Outline each blood parasite and name the species.
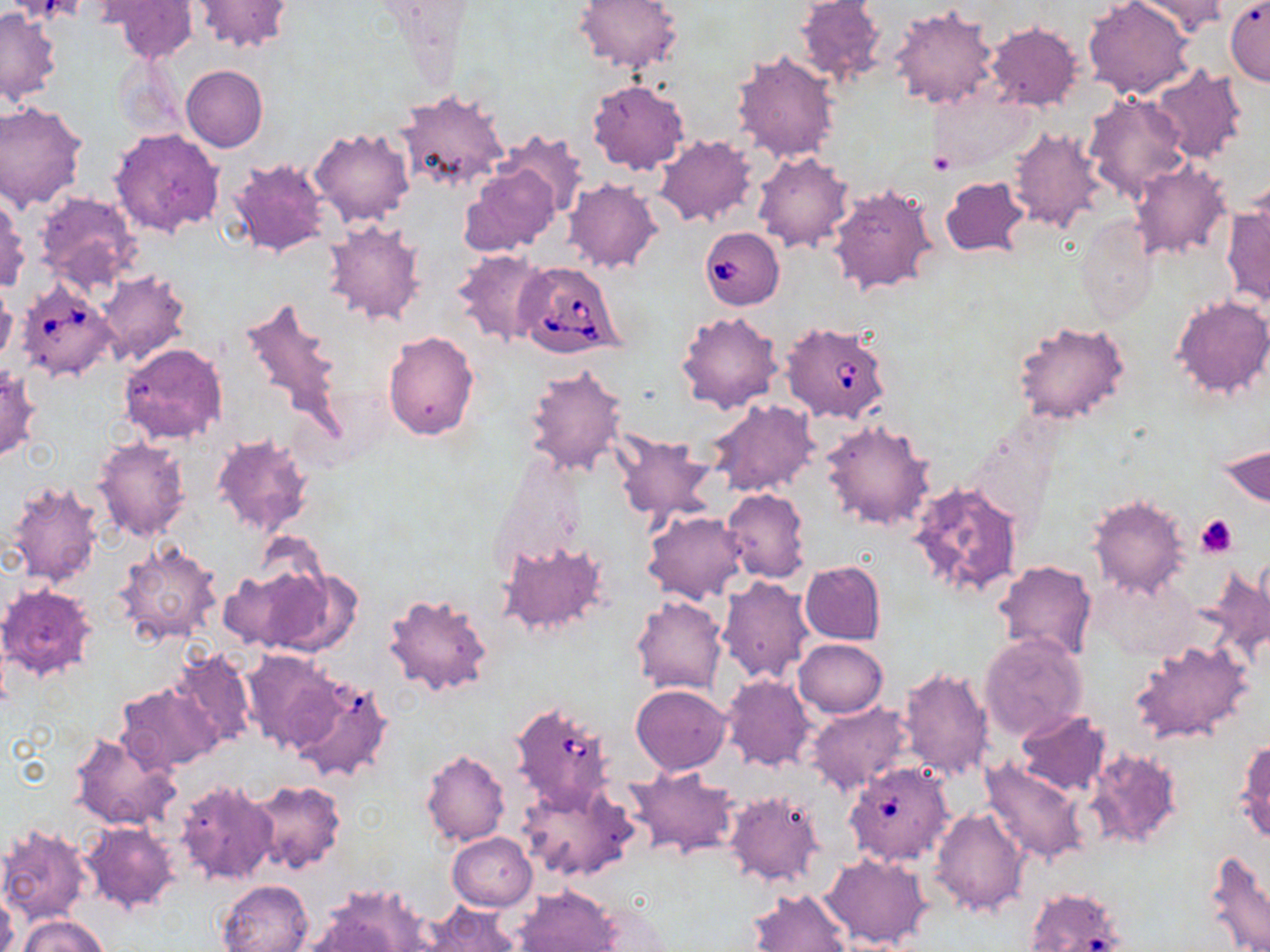
Approximate bounding boxes as named x1/y1/x2/y2 corners in pixels.
Babesia divergens-infected red blood cells: (x1=698, y1=228, x2=784, y2=310), (x1=515, y1=261, x2=624, y2=360), (x1=16, y1=280, x2=119, y2=383), (x1=780, y1=322, x2=891, y2=425), (x1=510, y1=701, x2=616, y2=810), (x1=844, y1=765, x2=957, y2=865), (x1=1031, y1=893, x2=1126, y2=952).
No Plasmodium falciparum, Plasmodium ovale, Plasmodium malariae, Plasmodium vivax, or Trypanosoma brucei observed.

slide-level diagnosis = Babesia divergens
field of view = single
stain = May-Grünwald-Giemsa
magnification = 1000x
platelet locations = approximate bounding boxes as named x1/y1/x2/y2 corners in pixels: (x1=928, y1=152, x2=954, y2=173), (x1=1196, y1=514, x2=1238, y2=557)
preparation = thin blood smear
uninfected red blood cell locations = approximate bounding boxes as named x1/y1/x2/y2 corners in pixels: (x1=192, y1=0, x2=293, y2=53), (x1=573, y1=0, x2=684, y2=73), (x1=793, y1=0, x2=886, y2=82), (x1=1082, y1=0, x2=1196, y2=100), (x1=1128, y1=0, x2=1230, y2=38), (x1=106, y1=1, x2=198, y2=64), (x1=1225, y1=1, x2=1270, y2=83), (x1=372, y1=2, x2=475, y2=44), (x1=890, y1=6, x2=999, y2=111), (x1=0, y1=7, x2=62, y2=103), (x1=985, y1=21, x2=1083, y2=111), (x1=732, y1=50, x2=840, y2=163), (x1=181, y1=65, x2=268, y2=151), (x1=1149, y1=65, x2=1247, y2=165), (x1=588, y1=79, x2=690, y2=175), (x1=929, y1=87, x2=1039, y2=174), (x1=394, y1=89, x2=508, y2=193), (x1=1083, y1=93, x2=1192, y2=204), (x1=0, y1=103, x2=87, y2=211), (x1=1006, y1=125, x2=1108, y2=234), (x1=108, y1=127, x2=225, y2=238), (x1=308, y1=127, x2=414, y2=227), (x1=494, y1=131, x2=588, y2=222), (x1=654, y1=135, x2=756, y2=227), (x1=753, y1=151, x2=854, y2=253), (x1=226, y1=157, x2=331, y2=260), (x1=1129, y1=163, x2=1233, y2=261), (x1=460, y1=167, x2=559, y2=256), (x1=941, y1=177, x2=1030, y2=258), (x1=563, y1=178, x2=664, y2=274), (x1=828, y1=184, x2=937, y2=296), (x1=33, y1=191, x2=141, y2=293), (x1=0, y1=195, x2=29, y2=293), (x1=1222, y1=204, x2=1270, y2=306), (x1=1075, y1=216, x2=1156, y2=321), (x1=322, y1=219, x2=427, y2=326), (x1=452, y1=248, x2=553, y2=347), (x1=95, y1=270, x2=191, y2=364), (x1=0, y1=285, x2=17, y2=366), (x1=234, y1=292, x2=350, y2=446), (x1=1170, y1=296, x2=1270, y2=400), (x1=675, y1=310, x2=783, y2=413), (x1=1012, y1=320, x2=1131, y2=426), (x1=383, y1=330, x2=480, y2=439), (x1=119, y1=342, x2=227, y2=445), (x1=0, y1=364, x2=41, y2=462), (x1=524, y1=364, x2=628, y2=480), (x1=707, y1=399, x2=818, y2=498), (x1=820, y1=420, x2=935, y2=531), (x1=211, y1=432, x2=315, y2=540), (x1=611, y1=432, x2=718, y2=530), (x1=92, y1=436, x2=191, y2=541), (x1=1220, y1=443, x2=1269, y2=506), (x1=6, y1=480, x2=103, y2=588), (x1=908, y1=480, x2=1025, y2=601), (x1=722, y1=489, x2=811, y2=583), (x1=1088, y1=493, x2=1190, y2=599), (x1=644, y1=511, x2=748, y2=604), (x1=501, y1=541, x2=607, y2=635), (x1=113, y1=543, x2=223, y2=647), (x1=992, y1=558, x2=1096, y2=665), (x1=256, y1=561, x2=360, y2=657), (x1=800, y1=561, x2=886, y2=644), (x1=1205, y1=563, x2=1270, y2=665), (x1=218, y1=564, x2=322, y2=652), (x1=1092, y1=573, x2=1198, y2=661), (x1=718, y1=575, x2=817, y2=684), (x1=0, y1=584, x2=98, y2=680), (x1=383, y1=591, x2=494, y2=698), (x1=631, y1=596, x2=726, y2=695), (x1=979, y1=632, x2=1090, y2=741), (x1=793, y1=639, x2=888, y2=718), (x1=1131, y1=639, x2=1254, y2=744), (x1=172, y1=649, x2=255, y2=748), (x1=241, y1=651, x2=343, y2=753), (x1=898, y1=667, x2=993, y2=781), (x1=721, y1=674, x2=817, y2=771), (x1=289, y1=676, x2=395, y2=785), (x1=117, y1=682, x2=224, y2=772), (x1=631, y1=685, x2=731, y2=774), (x1=804, y1=701, x2=910, y2=796), (x1=1014, y1=710, x2=1112, y2=797), (x1=69, y1=731, x2=181, y2=830), (x1=1235, y1=737, x2=1270, y2=843), (x1=1086, y1=747, x2=1184, y2=850), (x1=421, y1=749, x2=510, y2=847), (x1=981, y1=759, x2=1089, y2=866), (x1=627, y1=766, x2=739, y2=858), (x1=175, y1=778, x2=280, y2=888), (x1=520, y1=779, x2=639, y2=883), (x1=246, y1=780, x2=347, y2=874), (x1=722, y1=789, x2=824, y2=888), (x1=931, y1=807, x2=1028, y2=917), (x1=78, y1=821, x2=182, y2=916), (x1=0, y1=823, x2=92, y2=925), (x1=447, y1=832, x2=537, y2=911), (x1=1205, y1=848, x2=1270, y2=952), (x1=820, y1=851, x2=933, y2=949), (x1=218, y1=879, x2=314, y2=952), (x1=312, y1=884, x2=436, y2=952), (x1=748, y1=887, x2=852, y2=952), (x1=514, y1=888, x2=620, y2=951), (x1=0, y1=889, x2=19, y2=952), (x1=417, y1=902, x2=520, y2=952), (x1=578, y1=902, x2=675, y2=951), (x1=18, y1=915, x2=108, y2=952)
modality = optical microscopy
image size = 1270×952 pixels